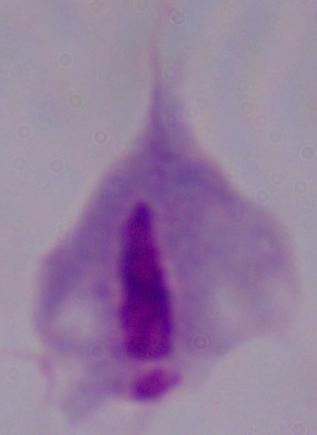 Photomicrograph. A trichomonad is shown. Captured at 1000x magnification.